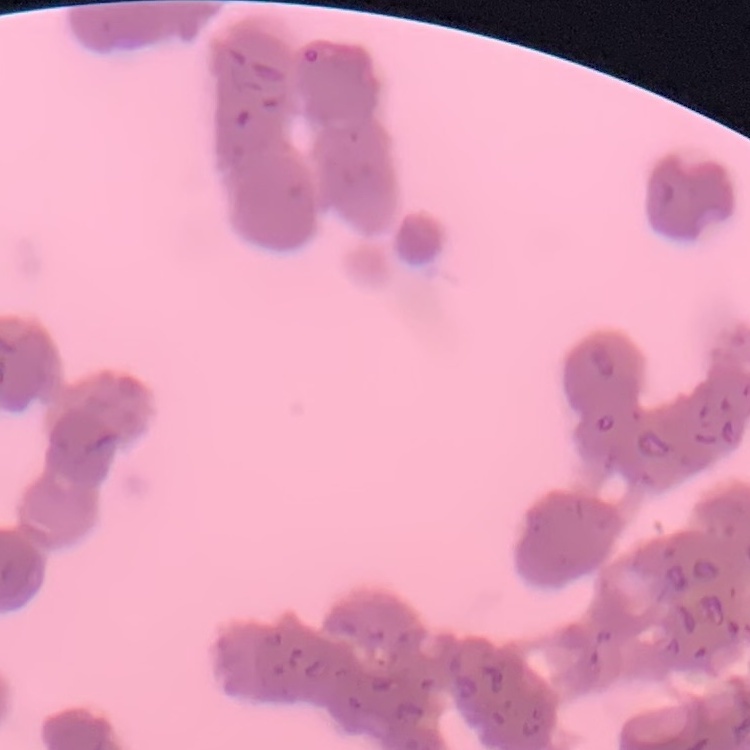
red blood cell morphology = rouleaux formation
preparation = thin blood film
image type = square crop of a larger photomicrograph
stain = Field's or Giemsa